Comment on the morphology of the erythrocytes.
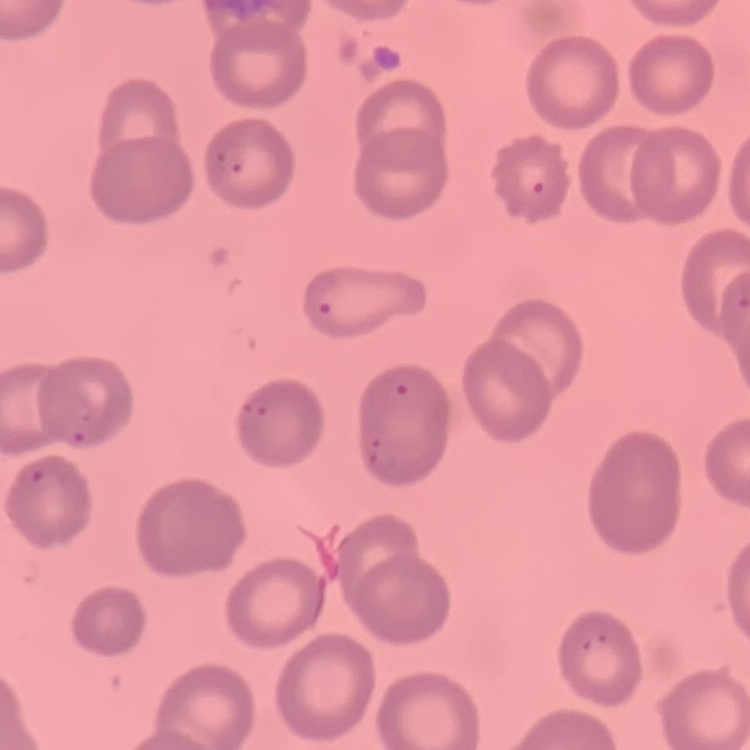
They show no rouleaux formation.

Thin blood smear. One tile cut from a larger photomicrograph. Field's or Giemsa stain.